Outline each blood parasite and name the species.
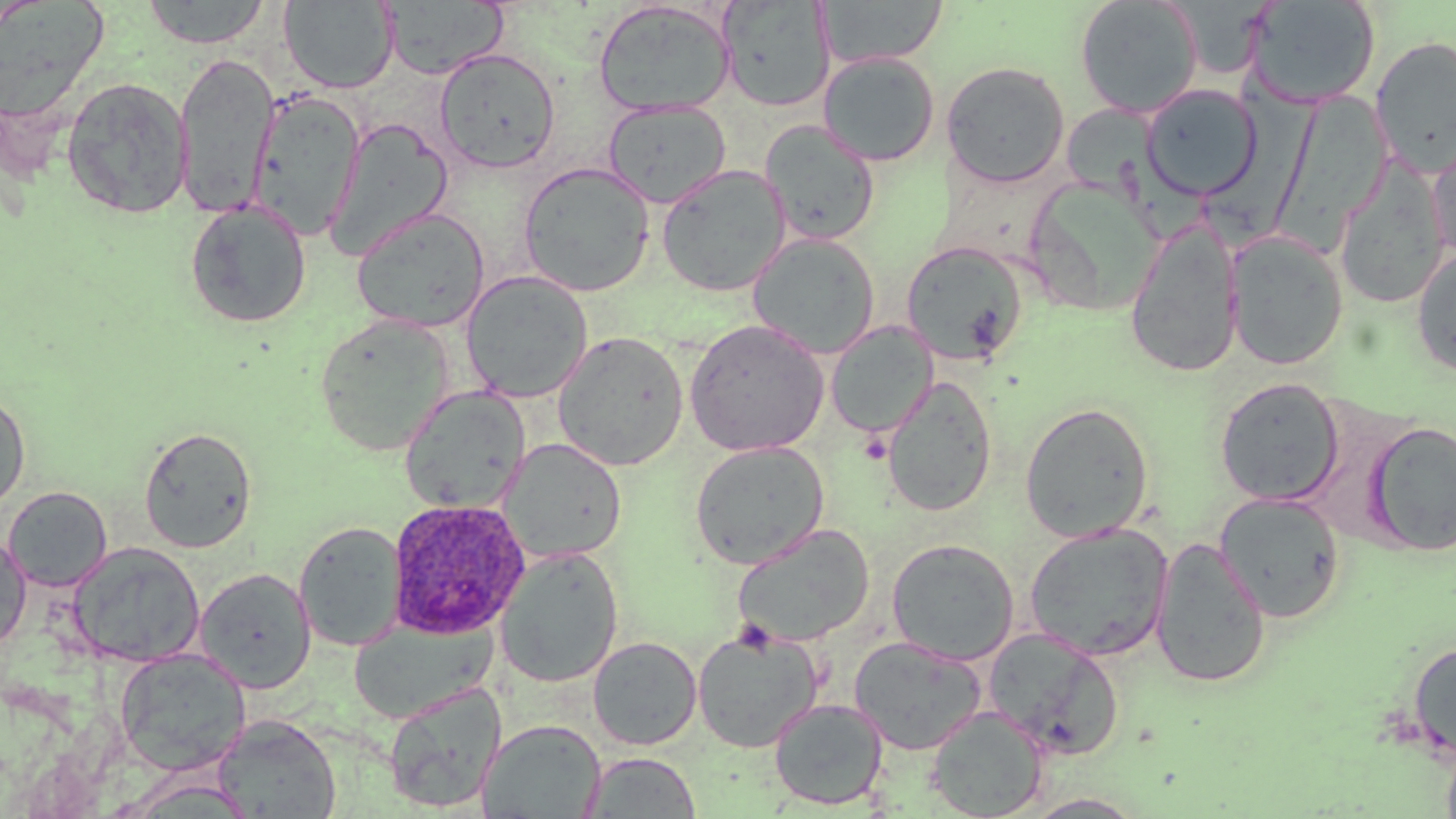
Approximate bounding boxes as [x1, y1, x2, y2] in pixels.
Plasmodium ovale-infected red blood cells: [387, 498, 530, 639].
No Plasmodium falciparum, Plasmodium malariae, Plasmodium vivax, Babesia divergens, or Trypanosoma brucei observed.

Summary:
  - Uninfected red blood cell locations: [141, 0, 272, 48], [817, 0, 948, 68], [1075, 0, 1203, 119], [0, 1, 109, 126], [279, 1, 399, 93], [380, 1, 508, 79], [593, 1, 736, 118], [717, 1, 835, 112], [1245, 1, 1381, 109], [1370, 35, 1456, 176], [434, 47, 560, 174], [173, 52, 280, 218], [819, 52, 940, 166], [941, 61, 1071, 188], [61, 77, 193, 219], [1140, 84, 1261, 198], [1207, 86, 1337, 245], [247, 90, 365, 240], [1278, 91, 1393, 239], [602, 99, 731, 209], [1070, 110, 1224, 249], [327, 116, 455, 258], [760, 120, 880, 246], [1427, 134, 1456, 265], [518, 161, 655, 297], [1334, 162, 1450, 307], [656, 164, 791, 297], [1031, 181, 1170, 312], [184, 200, 312, 329], [351, 207, 490, 333], [1124, 223, 1242, 378], [1225, 230, 1348, 370], [748, 232, 880, 359], [901, 241, 1028, 367], [1411, 248, 1456, 378], [461, 270, 593, 402], [313, 314, 455, 457], [685, 319, 829, 456], [825, 321, 937, 438], [552, 330, 690, 471], [881, 375, 997, 517], [1214, 377, 1345, 506], [399, 386, 531, 514], [0, 390, 31, 515], [1019, 401, 1155, 542], [1365, 420, 1456, 556], [138, 425, 257, 553], [499, 438, 627, 563], [689, 440, 830, 569], [3, 486, 112, 592], [1213, 491, 1347, 623], [294, 520, 406, 651], [731, 523, 875, 647], [1024, 523, 1173, 662], [0, 532, 32, 653], [1150, 537, 1272, 688], [887, 538, 1020, 665], [68, 542, 205, 667], [495, 547, 624, 687], [194, 568, 315, 694], [347, 619, 495, 723], [693, 626, 822, 753], [982, 627, 1124, 759], [849, 635, 987, 755], [588, 636, 702, 750], [1406, 640, 1456, 762], [114, 649, 251, 776], [382, 683, 505, 813], [769, 697, 888, 811], [926, 705, 1048, 819], [212, 715, 341, 819], [478, 719, 606, 819], [1441, 737, 1456, 819], [582, 752, 702, 817], [1022, 793, 1149, 818]
  - Slide-level diagnosis: Plasmodium ovale
  - Preparation: thin blood film
  - Magnification: 1000x
  - Modality: light microscopy
  - Field of view: one of a larger specimen
  - Image size: 1456×819 pixels
  - Stain: May-Grünwald-Giemsa